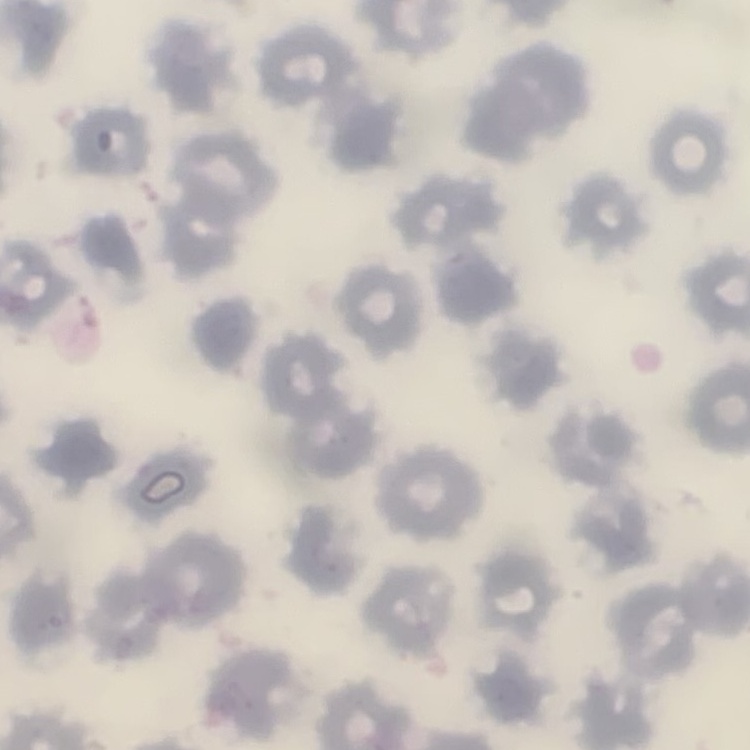

Summary:
  - Red blood cell morphology: no rouleaux formation
  - Stain: Field's or Giemsa
  - Image type: square crop of a larger photomicrograph
  - Preparation: thin blood film